Identify the parasite.
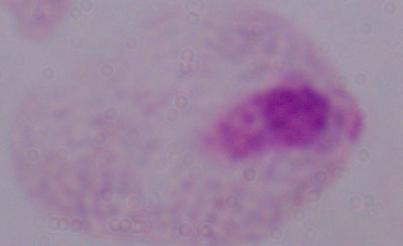

This is a trichomonad.

Captured at 1000x magnification. Photomicrograph.